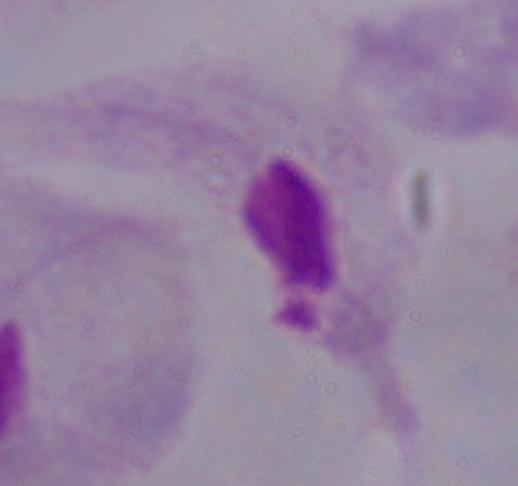 Captured at 1000x magnification. A trichomonad is seen. Micrograph.